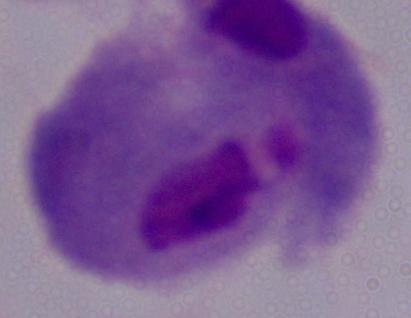
1000x magnification. Micrograph. A trichomonad is seen.